Assess the morphology of the red blood cells.
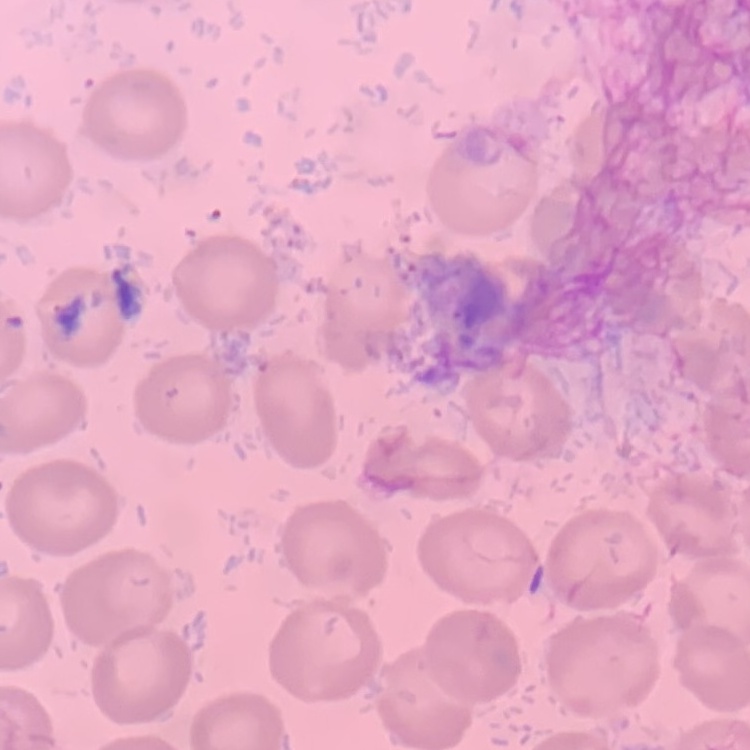

No rouleaux formation.

Summary:
  - Preparation: thin blood film
  - Image type: one tile cut from a larger photomicrograph
  - Stain: Field's or Giemsa